Report the malaria status of this cell.
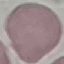
Uninfected.

Summary:
  - Capture: smartphone through the microscope eyepiece
  - Stain: Giemsa
  - Preparation: thin blood film
  - Image type: cell patch, automatically extracted from a larger field of view and resized to 64 × 64 pixels